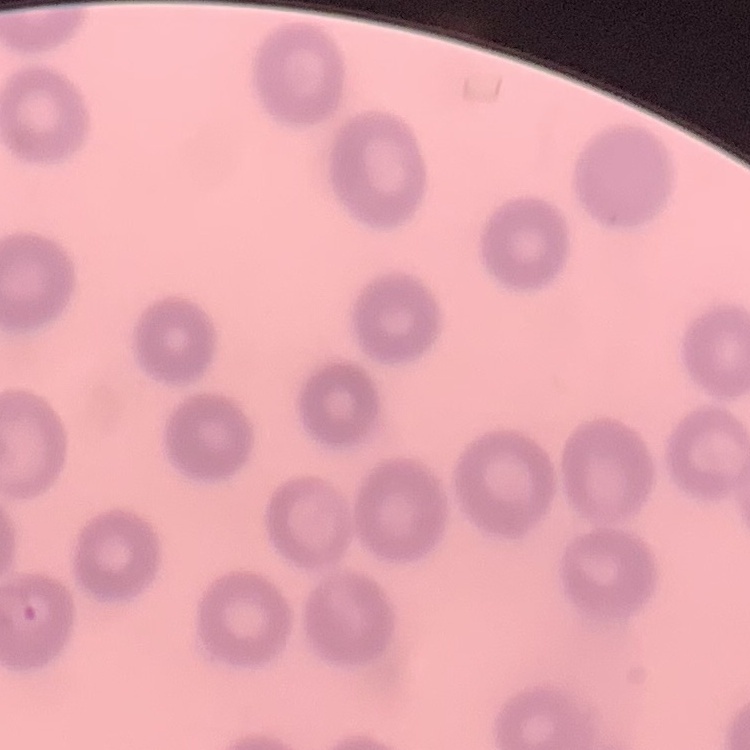
The red blood cells show no rouleaux formation. Field's or Giemsa stain. Thin peripheral smear. One tile cut from a larger photomicrograph.